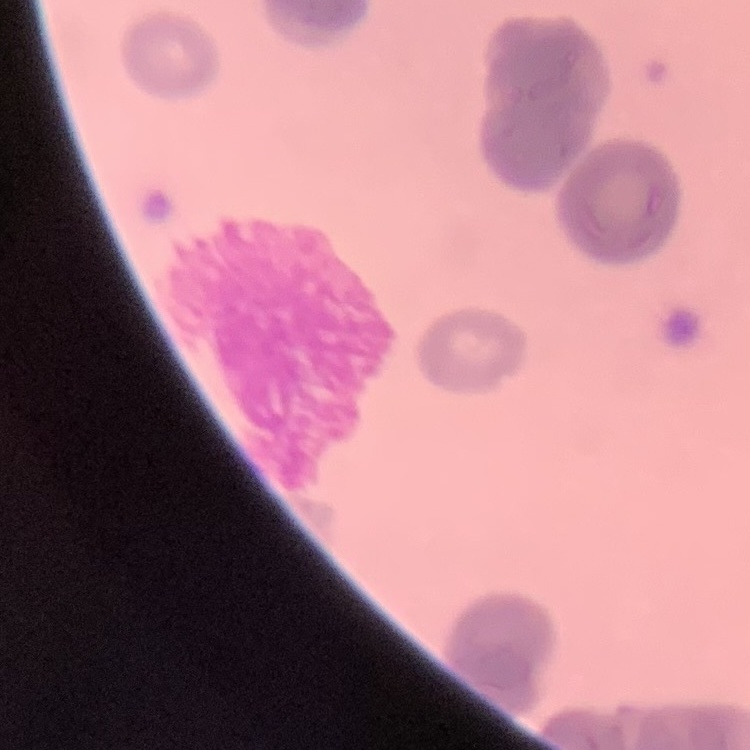

The red blood cells exhibit rouleaux formation. Square crop of a larger photomicrograph. Thin blood film. Stained with either Field's or Giemsa.